Comment on the morphology of the erythrocytes.
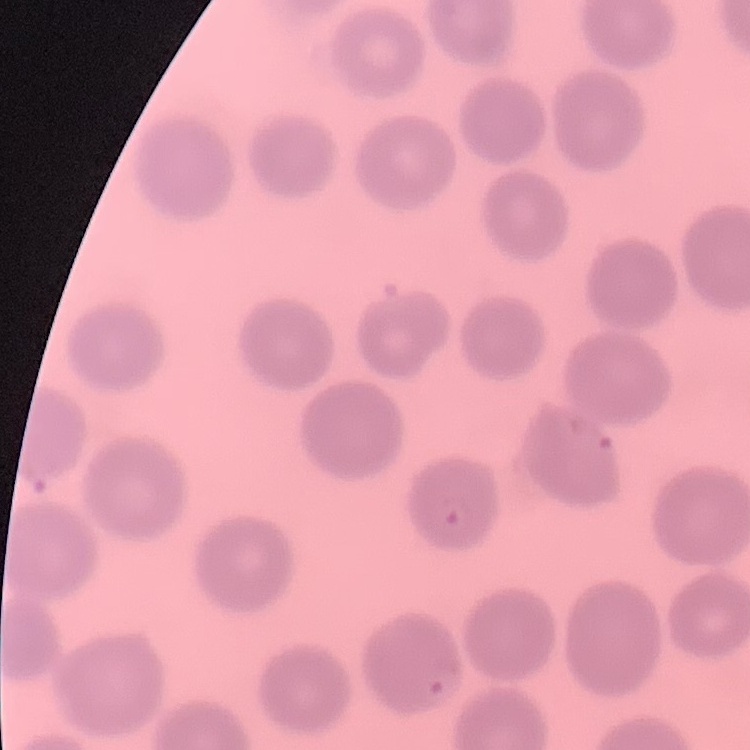
They show no rouleaux formation.

Summary:
  - Preparation: thin blood film
  - Stain: Field's or Giemsa
  - Image type: square crop of a larger photomicrograph